Assess this cell for malaria.
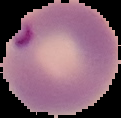

Parasitized.

Image is 121×118 pixels. Segmented cell region on a black background. From a thin blood smear.